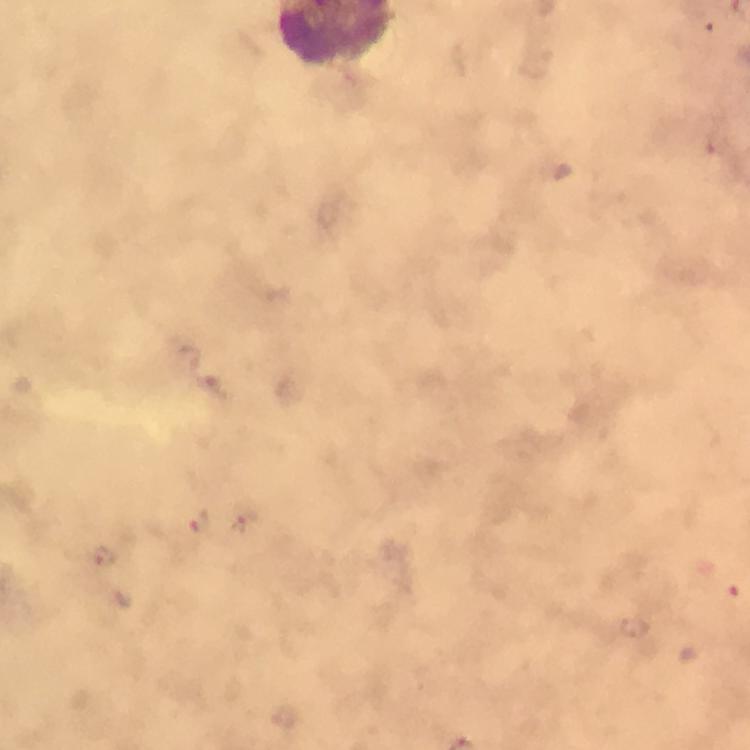
Approximate object centers, in pixels from the top-left corner. Malaria parasite locations: (x=200, y=520), (x=239, y=526), (x=103, y=557), (x=635, y=627). Image is 750×750 pixels. Thick blood film. Cropped region of a single field of view. Giemsa-stained preparation. Immersion oil applied. From a diagnostic examination for malaria. At 100x magnification. Photographed through the microscope with a smartphone camera.